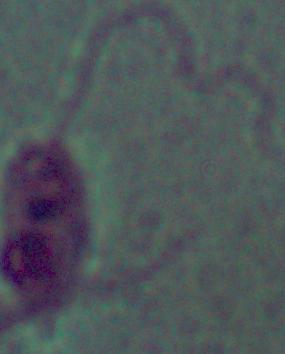

A Leishmania parasite is seen. Captured at 1000x magnification. Photomicrograph.